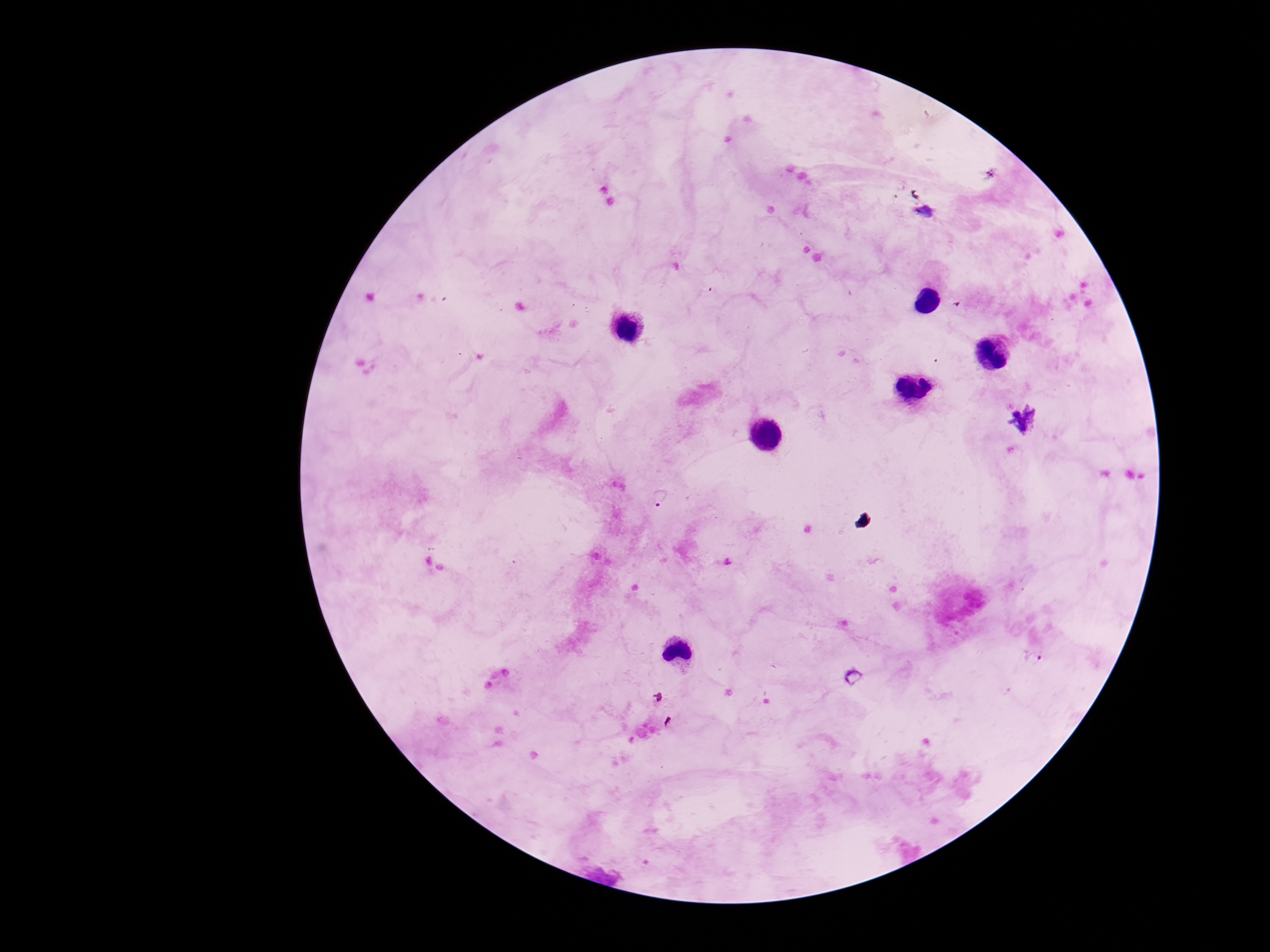

image size = 1270×952 pixels
magnification = 100x
capture = smartphone camera through the microscope eyepiece
field of view = one from this slide
stain = Giemsa
patient malaria status = positive
preparation = thick blood smear
Plasmodium parasite locations = approximate centers as (x, y) in pixels: (661, 498)